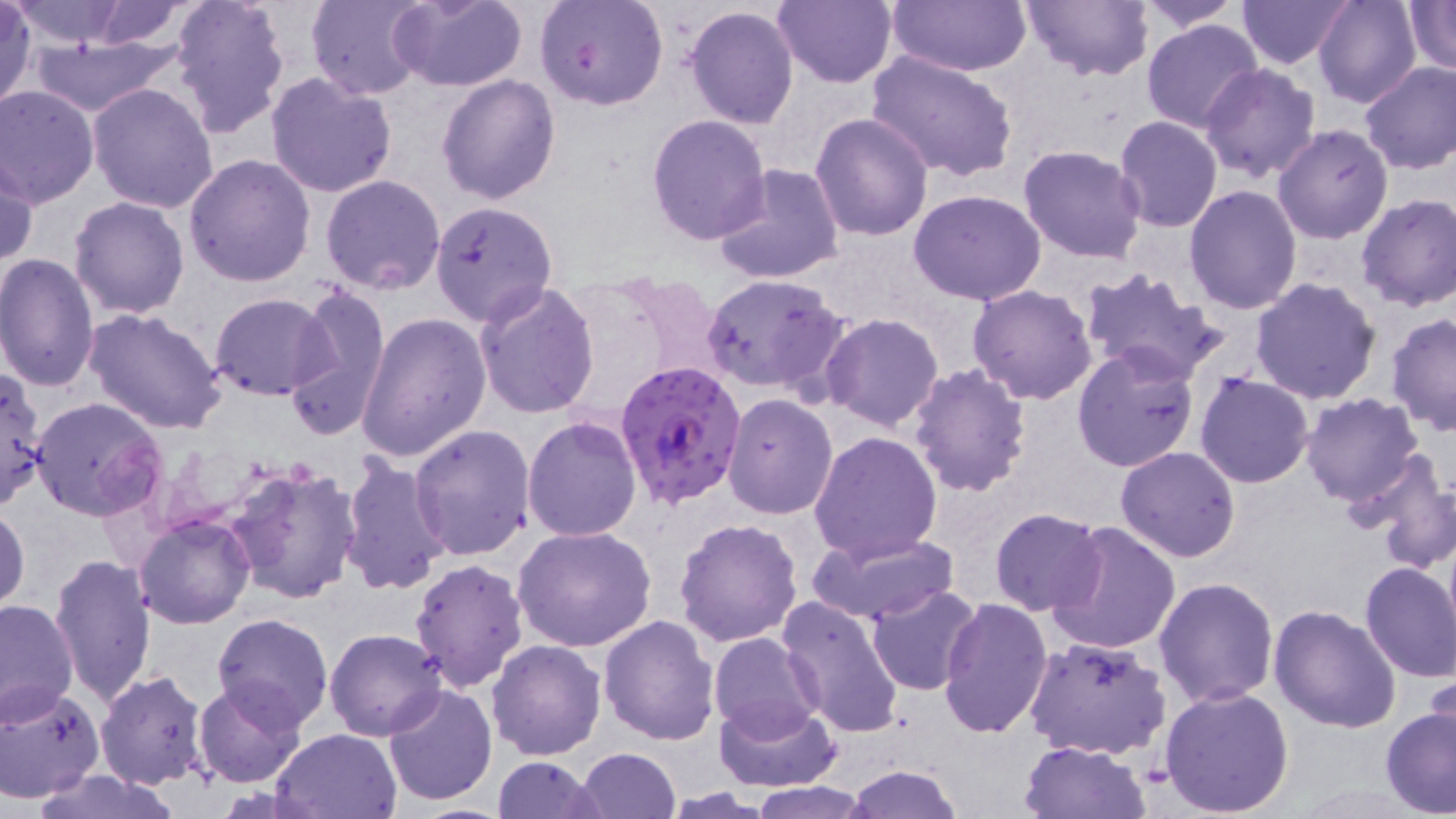

Summary:
  - Coordinate format: approximate bounding boxes as named x1/y1/x2/y2 corners in pixels
  - Plasmodium falciparum-infected red blood cell locations: (x1=612, y1=359, x2=748, y2=511)
  - Uninfected red blood cell locations: (x1=169, y1=0, x2=290, y2=136), (x1=307, y1=0, x2=432, y2=100), (x1=387, y1=0, x2=527, y2=91), (x1=538, y1=0, x2=669, y2=111), (x1=771, y1=0, x2=897, y2=89), (x1=1018, y1=0, x2=1152, y2=80), (x1=1133, y1=0, x2=1247, y2=30), (x1=1237, y1=0, x2=1353, y2=69), (x1=1314, y1=0, x2=1421, y2=107), (x1=6, y1=1, x2=135, y2=48), (x1=70, y1=1, x2=200, y2=49), (x1=887, y1=1, x2=1032, y2=76), (x1=1404, y1=1, x2=1455, y2=76), (x1=0, y1=5, x2=36, y2=111), (x1=683, y1=6, x2=800, y2=130), (x1=1141, y1=19, x2=1265, y2=134), (x1=22, y1=33, x2=183, y2=116), (x1=867, y1=49, x2=1019, y2=183), (x1=1359, y1=62, x2=1456, y2=174), (x1=1199, y1=64, x2=1321, y2=184), (x1=265, y1=74, x2=399, y2=198), (x1=437, y1=76, x2=562, y2=205), (x1=87, y1=82, x2=220, y2=213), (x1=0, y1=84, x2=99, y2=206), (x1=809, y1=111, x2=934, y2=242), (x1=646, y1=114, x2=772, y2=247), (x1=1113, y1=116, x2=1223, y2=233), (x1=1273, y1=124, x2=1394, y2=243), (x1=1019, y1=143, x2=1147, y2=264), (x1=183, y1=154, x2=315, y2=287), (x1=1, y1=155, x2=37, y2=269), (x1=713, y1=165, x2=844, y2=285), (x1=321, y1=174, x2=448, y2=294), (x1=1184, y1=186, x2=1302, y2=316), (x1=908, y1=189, x2=1048, y2=307), (x1=1355, y1=192, x2=1455, y2=311), (x1=69, y1=195, x2=192, y2=318), (x1=429, y1=199, x2=559, y2=325), (x1=0, y1=253, x2=100, y2=394), (x1=1077, y1=267, x2=1229, y2=386), (x1=701, y1=273, x2=849, y2=397), (x1=1249, y1=277, x2=1382, y2=406), (x1=474, y1=283, x2=601, y2=417), (x1=285, y1=285, x2=392, y2=442), (x1=967, y1=285, x2=1097, y2=404), (x1=211, y1=293, x2=333, y2=400), (x1=364, y1=296, x2=599, y2=439), (x1=84, y1=306, x2=228, y2=434), (x1=1386, y1=312, x2=1456, y2=435), (x1=357, y1=313, x2=490, y2=462), (x1=820, y1=313, x2=945, y2=431), (x1=1071, y1=345, x2=1201, y2=474), (x1=908, y1=363, x2=1032, y2=498), (x1=0, y1=369, x2=49, y2=510), (x1=1195, y1=373, x2=1315, y2=488), (x1=721, y1=393, x2=837, y2=520), (x1=1300, y1=393, x2=1426, y2=509), (x1=29, y1=396, x2=166, y2=521), (x1=521, y1=415, x2=643, y2=541), (x1=409, y1=423, x2=535, y2=560), (x1=809, y1=430, x2=943, y2=563), (x1=1115, y1=446, x2=1242, y2=563), (x1=1351, y1=453, x2=1456, y2=572), (x1=337, y1=455, x2=452, y2=597), (x1=225, y1=461, x2=364, y2=605), (x1=0, y1=503, x2=29, y2=617), (x1=989, y1=507, x2=1107, y2=616), (x1=134, y1=513, x2=255, y2=628), (x1=674, y1=518, x2=803, y2=649), (x1=1046, y1=521, x2=1181, y2=656), (x1=512, y1=525, x2=656, y2=652), (x1=805, y1=528, x2=962, y2=625), (x1=50, y1=554, x2=157, y2=707), (x1=410, y1=558, x2=528, y2=691), (x1=1358, y1=561, x2=1456, y2=682), (x1=1153, y1=576, x2=1279, y2=708), (x1=867, y1=585, x2=982, y2=696), (x1=775, y1=595, x2=907, y2=740), (x1=937, y1=598, x2=1053, y2=739), (x1=0, y1=599, x2=77, y2=725), (x1=1268, y1=605, x2=1400, y2=735), (x1=212, y1=613, x2=332, y2=732), (x1=598, y1=615, x2=720, y2=745), (x1=323, y1=628, x2=448, y2=741), (x1=708, y1=629, x2=824, y2=742), (x1=1023, y1=635, x2=1173, y2=760), (x1=485, y1=639, x2=606, y2=760), (x1=1425, y1=666, x2=1456, y2=771), (x1=95, y1=670, x2=210, y2=790), (x1=192, y1=679, x2=309, y2=789), (x1=0, y1=683, x2=106, y2=803), (x1=383, y1=683, x2=498, y2=806), (x1=1160, y1=684, x2=1294, y2=815), (x1=712, y1=698, x2=838, y2=792), (x1=1381, y1=704, x2=1456, y2=816), (x1=270, y1=727, x2=403, y2=818), (x1=1020, y1=739, x2=1151, y2=819), (x1=574, y1=748, x2=683, y2=819), (x1=492, y1=756, x2=602, y2=818), (x1=845, y1=764, x2=964, y2=818), (x1=27, y1=770, x2=181, y2=819), (x1=748, y1=784, x2=874, y2=818)
  - Slide-level diagnosis: Plasmodium falciparum
  - Image size: 1456×819 pixels
  - Stain: May-Grünwald-Giemsa
  - Modality: light microscopy
  - Magnification: 1000x
  - Preparation: thin blood smear
  - Field of view: one of a larger specimen